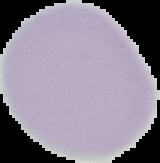
Cell region segmented out of the field of view; the surrounding area is masked to black. From a thin blood smear. Result: negative for Plasmodium parasites. Image is 160×163 pixels.